Report the malaria status of this cell.
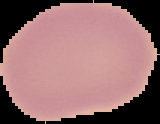
It is uninfected.

{
  "image_type": "segmented cell region with the area outside set to black",
  "preparation": "thin blood film",
  "image_size": "160×124 pixels"
}